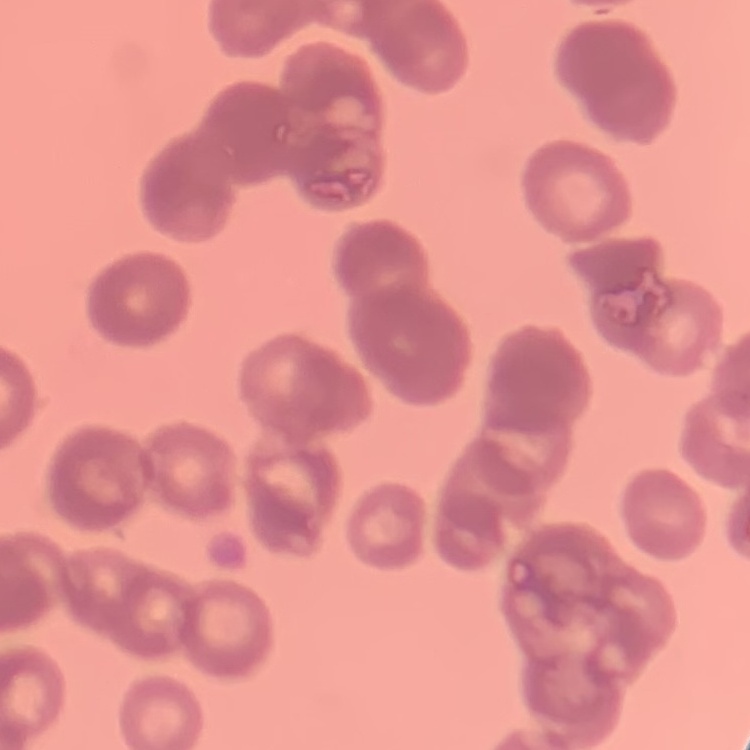

{
  "erythrocyte_morphology": "rouleaux formation",
  "preparation": "thin blood film",
  "image_type": "one tile cut from a larger photomicrograph",
  "stain": "Field's or Giemsa"
}